Outline every artifact (platelet-like body, stain precipitate, or debris).
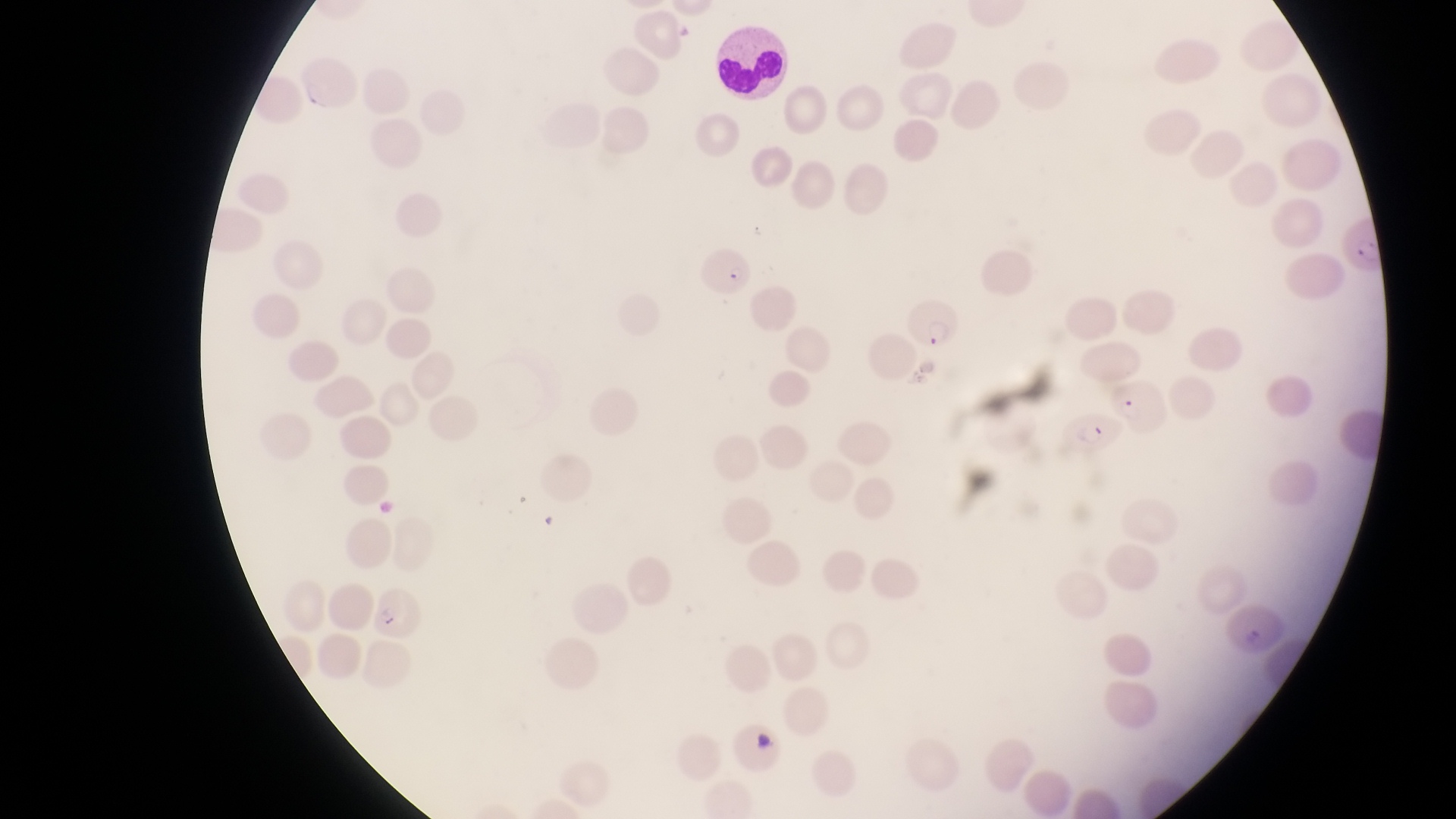

Approximate bounding boxes as (left, top, right, bottom) in pixels.
Artifacts (platelet-like body, stain precipitate, or debris): (752, 732, 782, 758).

Parasitised red blood cell locations: (1344, 219, 1393, 282), (692, 240, 756, 298), (905, 293, 960, 353), (1107, 378, 1173, 436), (1062, 403, 1114, 455), (370, 584, 420, 640). Leukocyte locations: (706, 24, 792, 104). Photographed through the eyepiece of an Olympus CX-23 microscope with a smartphone camera. At a magnification of 1000x. One field of view. Thin blood smear. Collected in Uganda. Image is 1456×819 pixels.